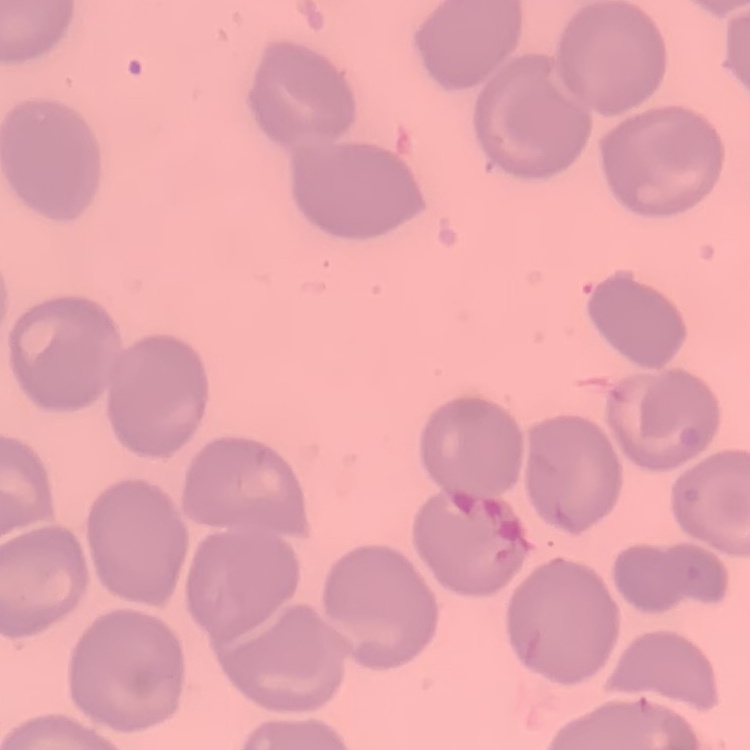
erythrocyte_morphology: no rouleaux formation
image_type: square crop of a larger photomicrograph
stain: Field's or Giemsa
preparation: thin blood film